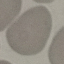

Summary:
  - Result: no malaria parasites seen
  - Preparation: thin smear
  - Image type: automatically extracted cell patch, resized to 64 × 64 pixels
  - Stain: Giemsa
  - Capture: smartphone camera at the microscope eyepiece